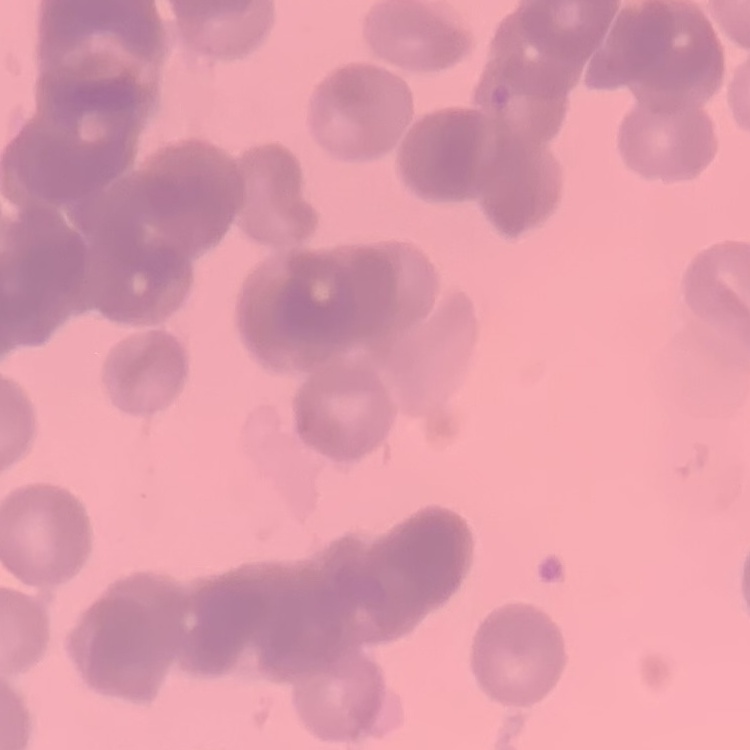

erythrocyte morphology = rouleaux formation
preparation = thin peripheral smear
stain = Field's or Giemsa
image type = one tile cut from a larger photomicrograph